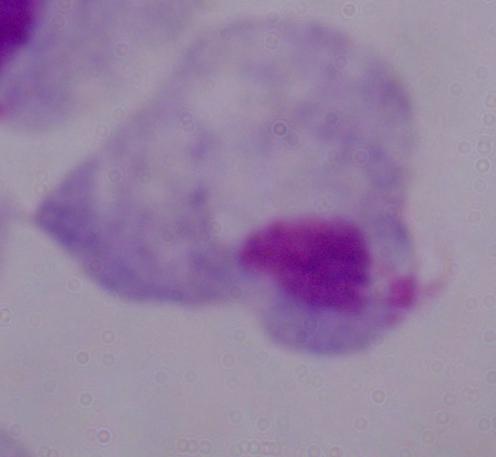

modality = photomicrograph
magnification = 1000x
identification = trichomonad